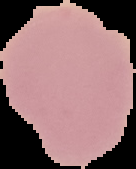 Malaria status: uninfected. Image is 136×169 pixels. The area outside the segmented cell region is set to black. From a thin blood film.